Classify this cell by malaria status.
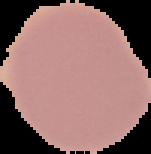

It is uninfected.

preparation = thin blood smear
image type = segmented cell region on a black background
image size = 151×154 pixels